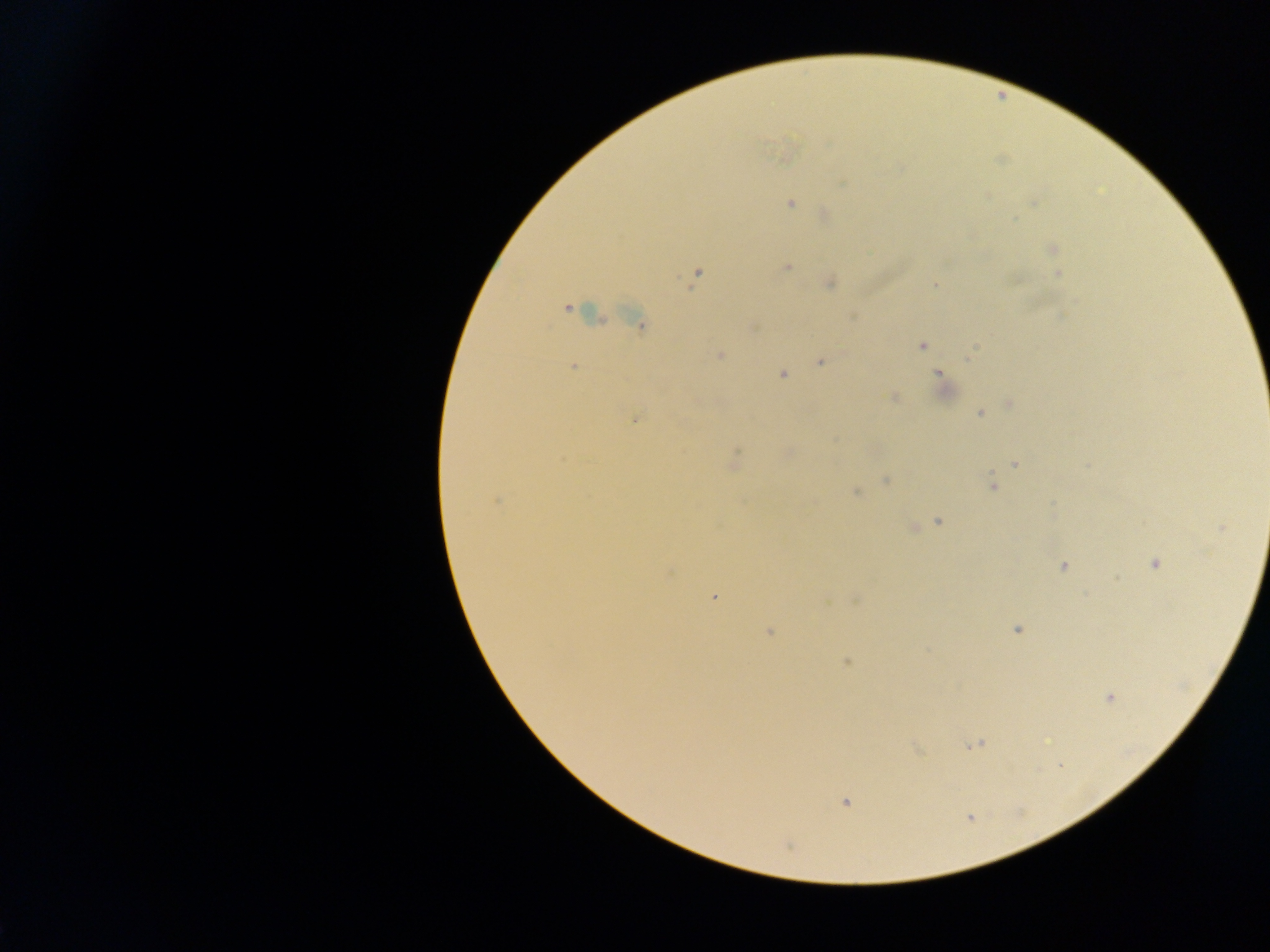
Approximate centers as [x, y] in pixels. Malaria parasite locations: [843, 184], [791, 204], [1052, 249], [787, 267], [1058, 273], [697, 274], [829, 284], [935, 284], [567, 308], [1062, 316], [640, 325], [922, 346], [971, 354], [719, 355], [820, 362], [573, 366], [781, 374], [939, 375], [893, 397], [1010, 404], [980, 414], [635, 420], [787, 453], [734, 459], [1014, 464], [886, 480], [992, 486], [856, 492], [497, 501], [939, 521], [913, 527], [1221, 528], [1155, 563], [1063, 566], [714, 596], [856, 599], [1017, 630], [770, 632], [847, 662], [1109, 698], [974, 745], [845, 802]. Photographed through a microscope with a mobile-phone camera. Sample from Ghana. One field of view. Thick blood smear. Image is 1270×952 pixels.